Comment on the morphology of the red blood cells.
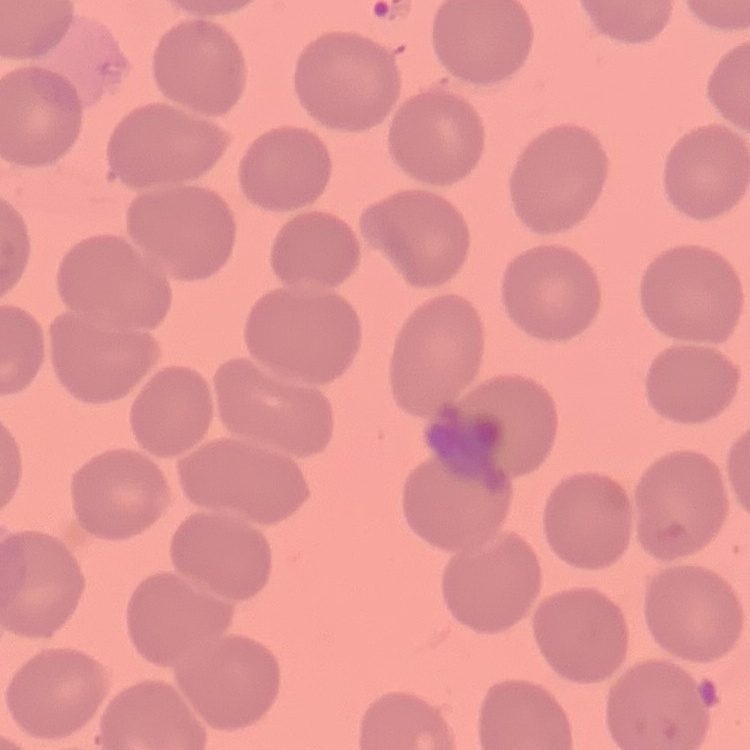

No rouleaux formation.

image_type: one tile cut from a larger photomicrograph
preparation: thin peripheral smear
stain: Field's or Giemsa